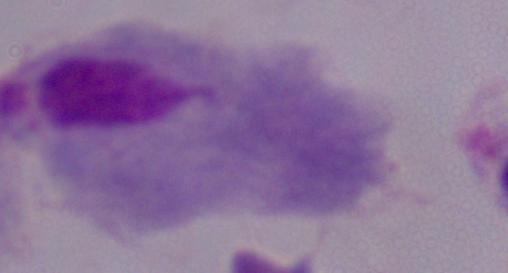

modality = photomicrograph
identification = trichomonad
magnification = 1000x